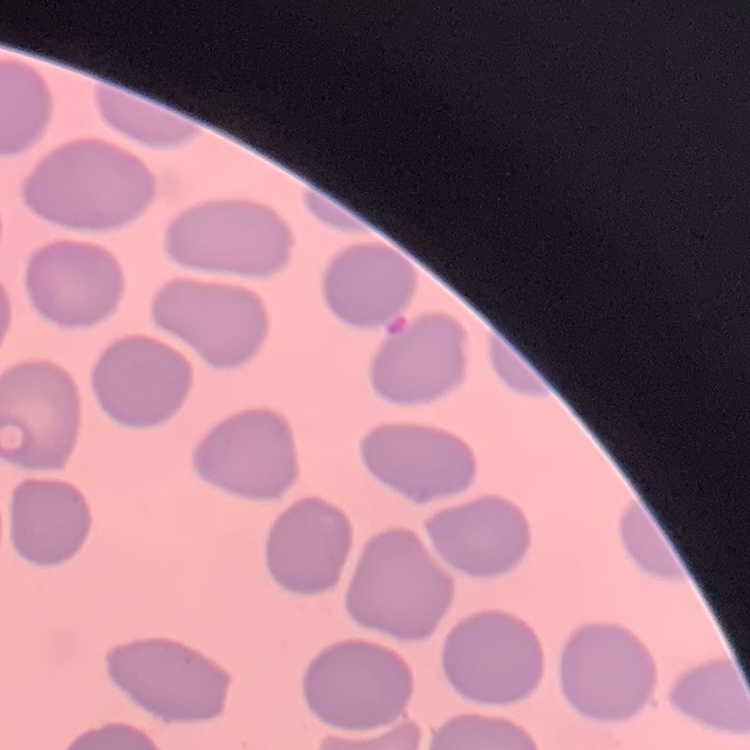
The erythrocytes show no rouleaux formation. Square crop of a larger photomicrograph. Field's or Giemsa stain. Thin peripheral smear.